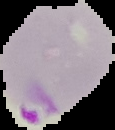
result = malaria parasites detected
image size = 115×130 pixels
preparation = thin blood smear
image type = segmented cell region with the area outside set to black